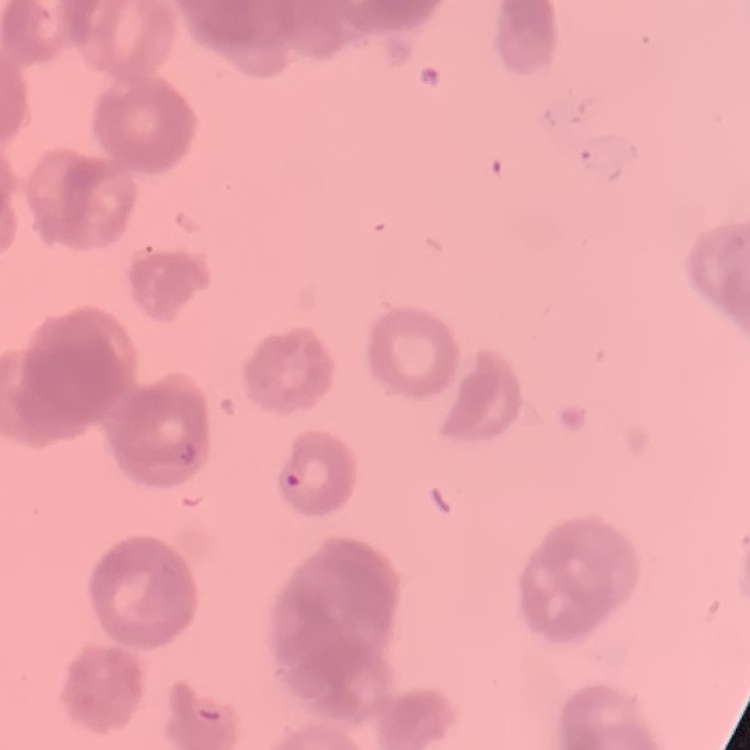 The erythrocytes exhibit rouleaux formation. Field's or Giemsa stain. Square crop of a larger photomicrograph. Thin peripheral smear.